Name the blood parasite species.
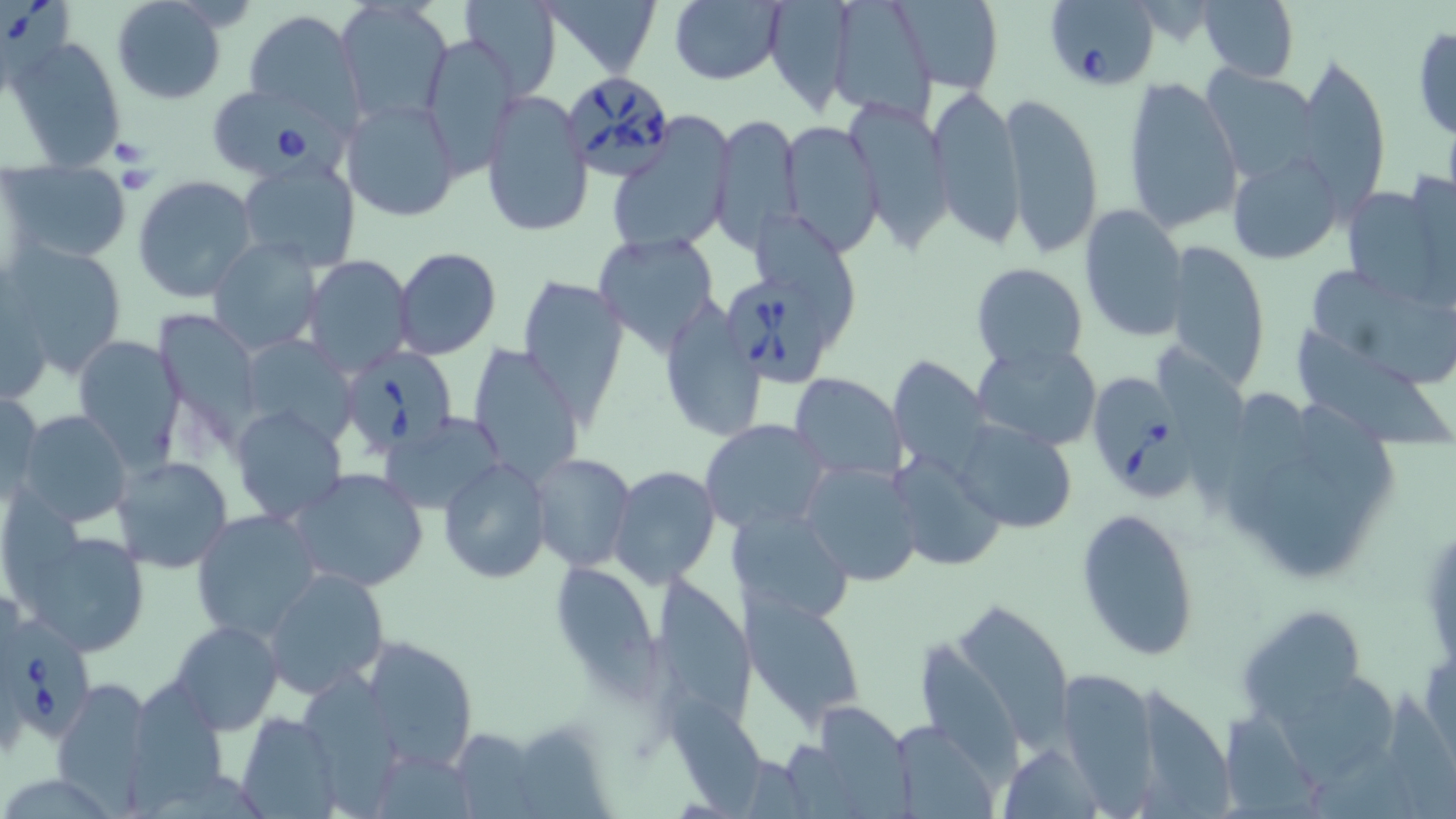

Babesia divergens.

Approximate bounding boxes as (x1, y1, x2, y2) in pixels. Babesia divergens-infected red blood cell locations: (1, 1, 78, 90), (1044, 1, 1159, 92), (563, 72, 676, 177), (210, 86, 335, 180), (727, 278, 827, 387), (342, 347, 457, 457), (1089, 377, 1195, 500), (6, 617, 98, 744). Uninfected red blood cell locations: (110, 0, 227, 107), (462, 0, 562, 98), (540, 0, 661, 75), (669, 0, 787, 85), (763, 0, 860, 115), (827, 0, 938, 123), (899, 0, 1004, 93), (336, 1, 452, 124), (1198, 1, 1297, 82), (241, 10, 361, 124), (1412, 26, 1456, 142), (6, 34, 128, 171), (419, 35, 520, 175), (1293, 55, 1392, 208), (1202, 65, 1320, 184), (1122, 75, 1244, 236), (926, 85, 1024, 245), (480, 91, 592, 238), (999, 92, 1105, 257), (341, 98, 461, 222), (843, 98, 953, 247), (610, 110, 735, 254), (710, 110, 803, 250), (777, 119, 882, 254), (1228, 147, 1345, 265), (237, 159, 360, 270), (4, 161, 131, 265), (133, 174, 259, 303), (1341, 183, 1448, 307), (1079, 204, 1188, 340), (756, 214, 857, 347), (593, 232, 721, 357), (208, 236, 322, 356), (1163, 240, 1272, 391), (4, 242, 129, 376), (393, 248, 502, 361), (301, 256, 412, 377), (970, 262, 1090, 370), (1312, 272, 1455, 387), (516, 275, 628, 422), (0, 277, 52, 409), (657, 294, 766, 442), (153, 311, 267, 439), (71, 333, 188, 469), (1297, 333, 1452, 456), (244, 339, 359, 444), (971, 341, 1102, 452), (468, 344, 584, 487), (886, 357, 992, 476), (788, 373, 906, 484), (1, 389, 44, 504), (1219, 390, 1315, 535), (1286, 395, 1402, 505), (229, 405, 348, 525), (16, 410, 133, 528), (380, 410, 507, 515), (949, 416, 1079, 533), (700, 417, 831, 535), (527, 452, 636, 573), (894, 452, 1006, 572), (112, 457, 233, 573), (438, 458, 552, 584), (802, 462, 923, 588), (1259, 465, 1365, 581), (287, 467, 429, 592), (610, 467, 719, 588), (1077, 503, 1201, 662), (726, 506, 855, 626), (191, 508, 323, 641), (16, 528, 152, 659), (556, 565, 660, 702), (262, 567, 389, 701), (654, 575, 756, 731), (743, 592, 867, 729), (945, 597, 1071, 749), (1237, 603, 1365, 722), (171, 620, 282, 733), (358, 638, 481, 774), (914, 643, 1027, 783), (1055, 667, 1161, 812), (300, 674, 414, 813), (52, 678, 158, 806), (1276, 679, 1399, 786), (125, 681, 228, 816), (1132, 688, 1239, 819), (666, 700, 783, 813), (821, 709, 920, 819), (235, 712, 340, 817), (1218, 712, 1326, 819), (891, 726, 993, 817), (519, 728, 612, 814), (996, 743, 1104, 816). Captured at 1000x magnification. Image is 1456×819 pixels. Optical microscopy. Thin blood film. May-Grünwald-Giemsa-stained preparation. One field of a larger specimen.